Comment on the morphology of the red blood cells.
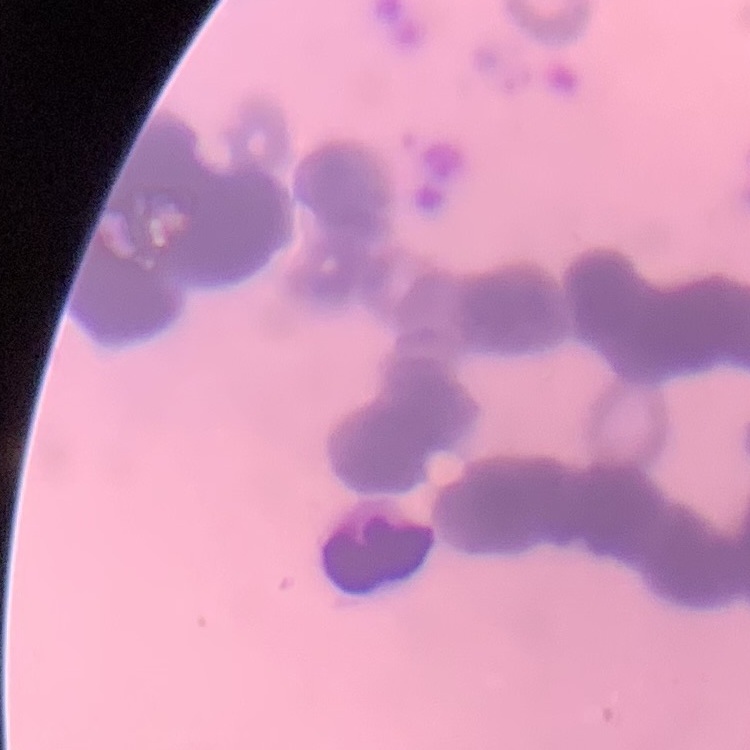
Rouleaux formation.

Stained with either Field's or Giemsa. Thin blood smear. Square crop of a larger photomicrograph.